Assess the morphology of the red blood cells.
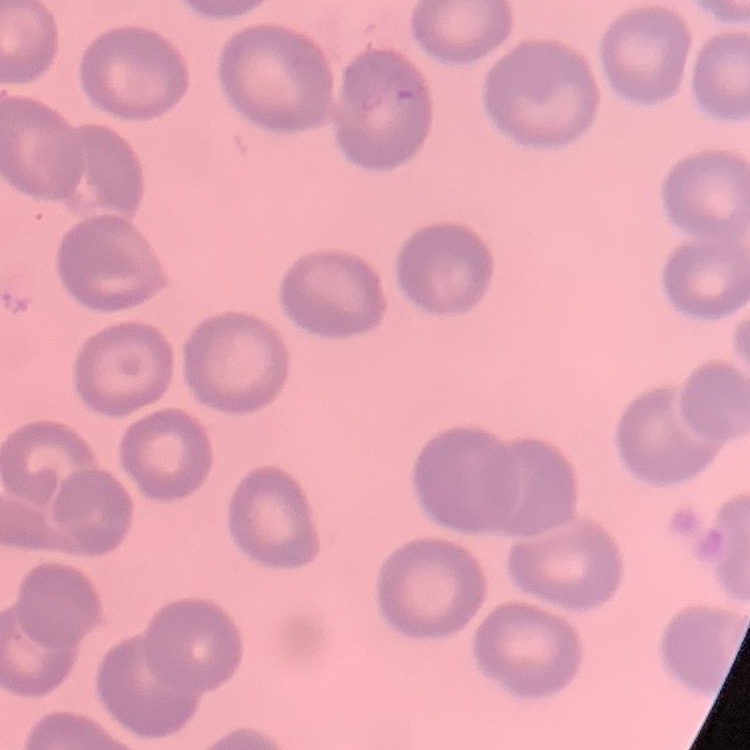
No rouleaux formation.

image type = square crop of a larger photomicrograph
preparation = thin peripheral smear
stain = Field's or Giemsa